Assess the morphology of the red blood cells.
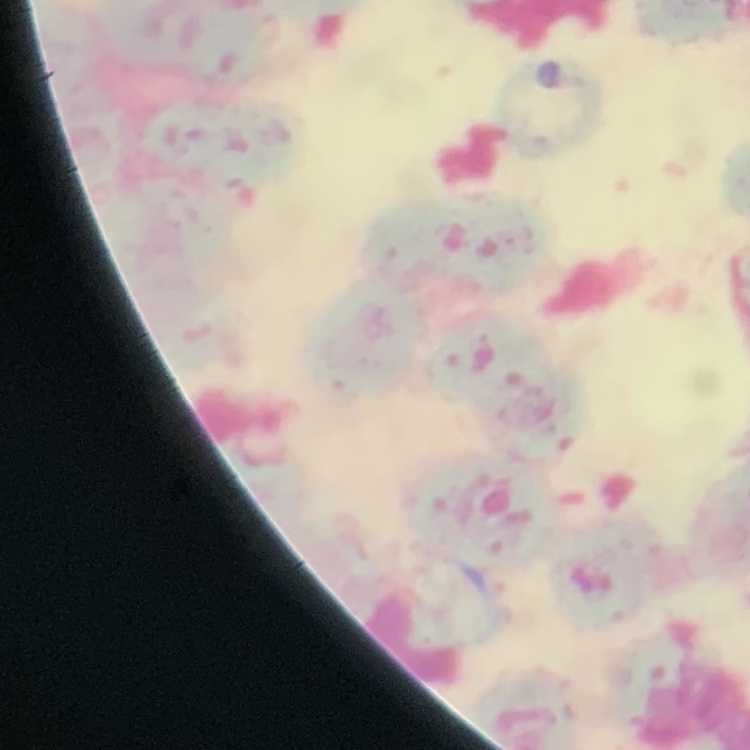

Rouleaux formation.

Summary:
  - Preparation: thin blood smear
  - Image type: one tile cut from a larger photomicrograph
  - Stain: Field's or Giemsa